Identify the parasite.
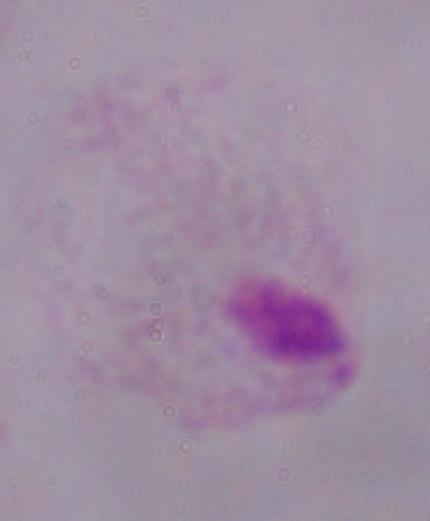
A trichomonad.

Photomicrograph. Captured at 1000x magnification.